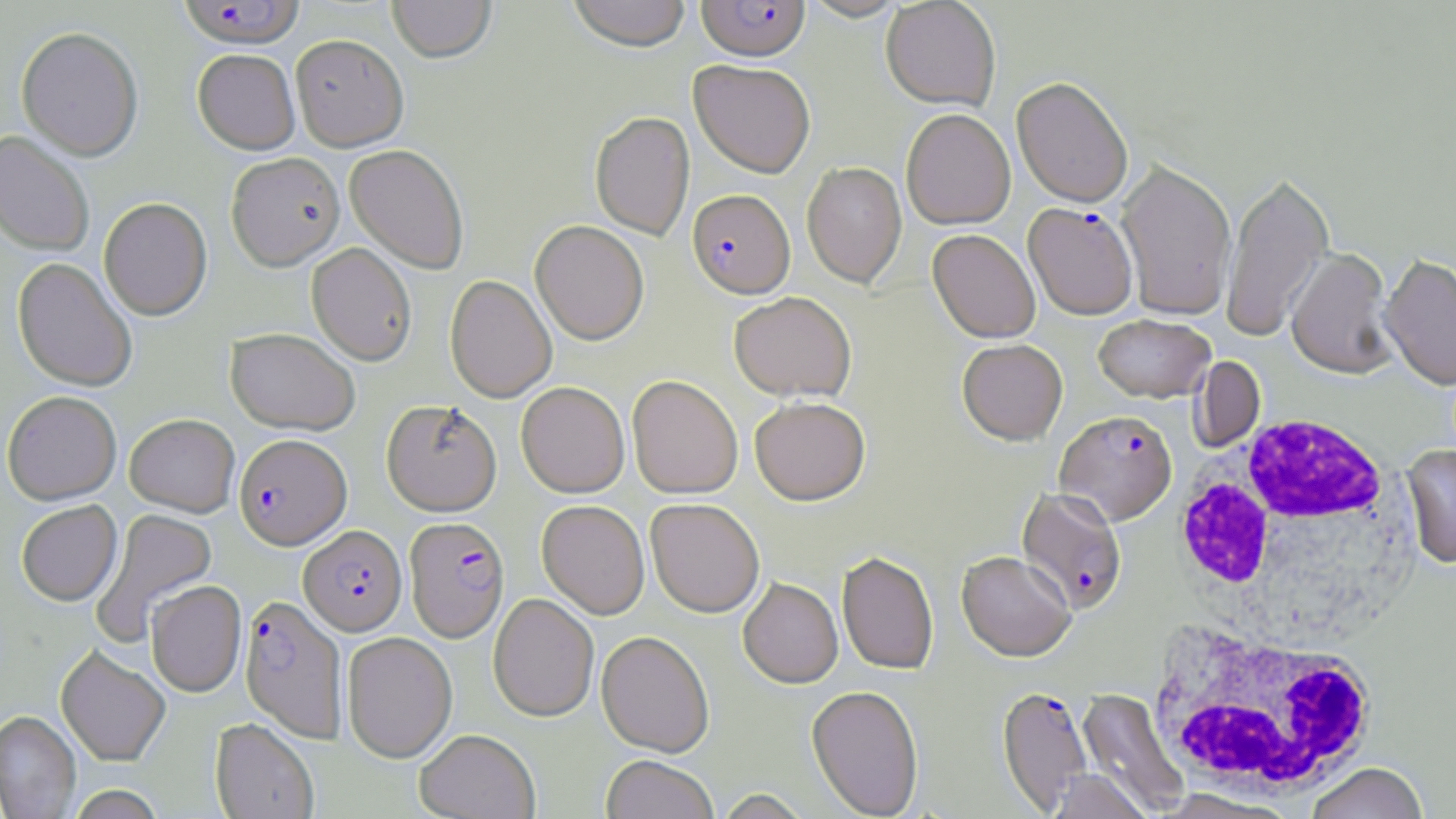
Summary:
  - Coordinate format: approximate bounding boxes as named x1/y1/x2/y2 corners in pixels
  - Plasmodium falciparum-infected red blood cell locations: (x1=178, y1=1, x2=304, y2=53), (x1=696, y1=1, x2=811, y2=65), (x1=687, y1=191, x2=796, y2=303), (x1=1024, y1=205, x2=1138, y2=322), (x1=1055, y1=412, x2=1178, y2=528), (x1=234, y1=435, x2=352, y2=551), (x1=1015, y1=487, x2=1127, y2=616), (x1=404, y1=517, x2=510, y2=643), (x1=299, y1=526, x2=407, y2=636), (x1=239, y1=595, x2=347, y2=742), (x1=997, y1=687, x2=1093, y2=814)
  - White blood cell locations: (x1=1169, y1=417, x2=1413, y2=634), (x1=1146, y1=626, x2=1383, y2=798), (x1=1074, y1=687, x2=1195, y2=819)
  - Uninfected red blood cell locations: (x1=387, y1=0, x2=497, y2=66), (x1=567, y1=0, x2=691, y2=55), (x1=802, y1=0, x2=910, y2=23), (x1=881, y1=1, x2=1001, y2=113), (x1=16, y1=29, x2=144, y2=163), (x1=291, y1=38, x2=409, y2=155), (x1=192, y1=52, x2=300, y2=158), (x1=688, y1=61, x2=815, y2=181), (x1=1011, y1=79, x2=1133, y2=210), (x1=901, y1=111, x2=1016, y2=231), (x1=589, y1=112, x2=695, y2=241), (x1=0, y1=132, x2=94, y2=257), (x1=344, y1=146, x2=469, y2=275), (x1=226, y1=155, x2=345, y2=274), (x1=802, y1=163, x2=907, y2=289), (x1=1116, y1=163, x2=1236, y2=322), (x1=1221, y1=173, x2=1334, y2=342), (x1=98, y1=199, x2=212, y2=322), (x1=530, y1=221, x2=649, y2=347), (x1=927, y1=231, x2=1040, y2=345), (x1=305, y1=244, x2=417, y2=367), (x1=1286, y1=250, x2=1400, y2=381), (x1=1379, y1=256, x2=1456, y2=391), (x1=12, y1=258, x2=137, y2=393), (x1=444, y1=276, x2=557, y2=404), (x1=728, y1=294, x2=857, y2=404), (x1=1093, y1=315, x2=1215, y2=403), (x1=226, y1=329, x2=359, y2=437), (x1=957, y1=341, x2=1068, y2=448), (x1=1190, y1=356, x2=1266, y2=453), (x1=627, y1=376, x2=743, y2=500), (x1=516, y1=382, x2=629, y2=498), (x1=2, y1=392, x2=122, y2=506), (x1=750, y1=399, x2=871, y2=508), (x1=381, y1=401, x2=502, y2=517), (x1=124, y1=415, x2=239, y2=517), (x1=1401, y1=444, x2=1456, y2=569), (x1=645, y1=500, x2=765, y2=619), (x1=16, y1=501, x2=122, y2=607), (x1=536, y1=501, x2=650, y2=620), (x1=90, y1=508, x2=218, y2=646), (x1=836, y1=553, x2=938, y2=676), (x1=956, y1=553, x2=1076, y2=665), (x1=738, y1=579, x2=843, y2=690), (x1=145, y1=581, x2=246, y2=698), (x1=488, y1=594, x2=599, y2=722), (x1=341, y1=632, x2=457, y2=763), (x1=596, y1=632, x2=714, y2=759), (x1=55, y1=646, x2=170, y2=767), (x1=806, y1=687, x2=924, y2=819), (x1=1077, y1=688, x2=1189, y2=816), (x1=0, y1=710, x2=81, y2=819), (x1=210, y1=718, x2=319, y2=819), (x1=415, y1=729, x2=541, y2=819), (x1=601, y1=757, x2=719, y2=819), (x1=1306, y1=763, x2=1429, y2=819), (x1=1046, y1=769, x2=1151, y2=819), (x1=66, y1=785, x2=165, y2=819), (x1=714, y1=789, x2=813, y2=819)
  - Slide-level diagnosis: Plasmodium falciparum
  - Magnification: 1000x
  - Image size: 1456×819 pixels
  - Field of view: one of a larger specimen
  - Stain: May-Grünwald-Giemsa
  - Preparation: thin blood smear
  - Modality: optical microscopy